State which cell type is depicted.
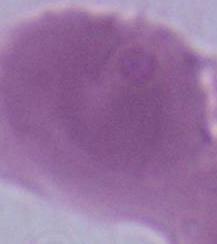
This is an erythrocyte.

Photomicrograph. Captured at 1000x magnification.